Comment on the morphology of the erythrocytes.
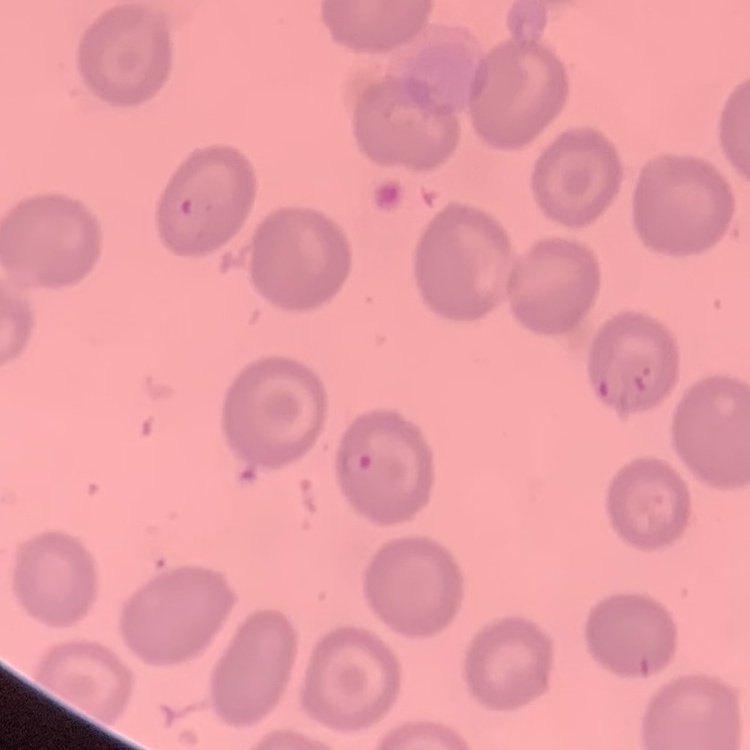
No rouleaux formation.

stain: Field's or Giemsa
image_type: square crop of a larger photomicrograph
preparation: thin peripheral smear